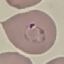

result: malaria parasites detected
preparation: thin smear
capture: smartphone through the microscope eyepiece
image_type: automatically extracted cell patch, resized to 64 × 64 pixels
stain: Giemsa